Name the parasite shown.
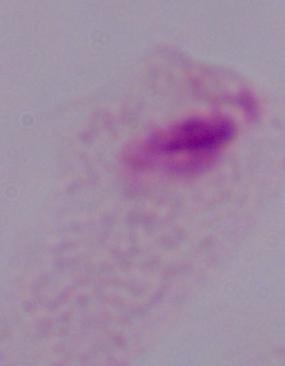

A trichomonad.

magnification = 1000x
modality = photomicrograph